Classify this cell by malaria status.
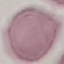
Uninfected.

Giemsa-stained preparation. Automatically extracted cell patch, resized to 64 × 64 pixels. Thin blood film. Acquired by smartphone through the microscope eyepiece.